Assess this cell for malaria.
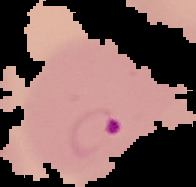
Parasitized.

Summary:
  - Image type: segmented cell region with the area outside set to black
  - Image size: 196×187 pixels
  - Preparation: thin blood film